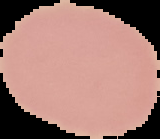
preparation = thin blood smear
image type = segmented cell region on a black background
image size = 160×139 pixels
malaria status = uninfected